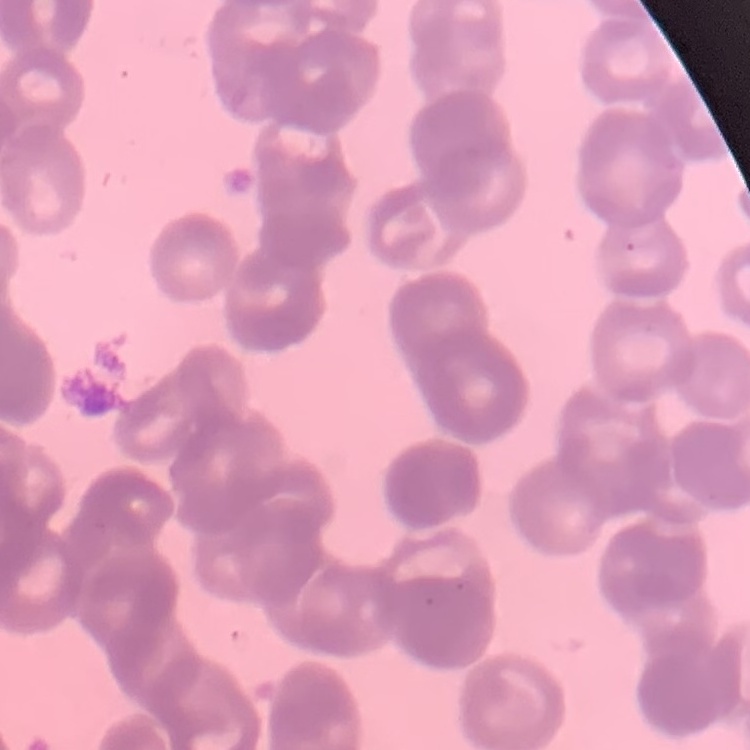
Summary:
  - Red blood cell morphology: rouleaux formation
  - Image type: square crop of a larger photomicrograph
  - Stain: Field's or Giemsa
  - Preparation: thin peripheral smear